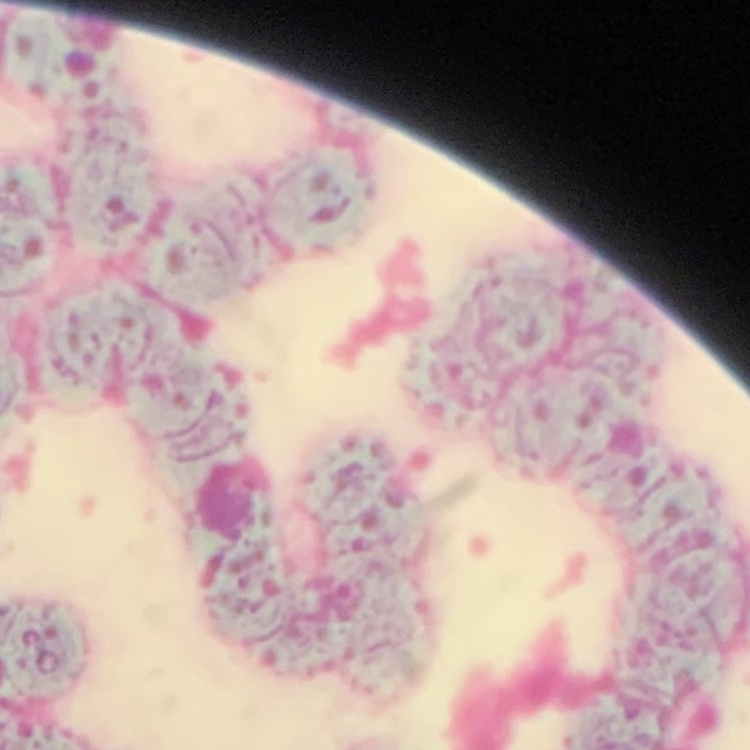

red blood cell morphology = rouleaux formation
preparation = thin blood smear
stain = Field's or Giemsa
image type = square crop of a larger photomicrograph